Give the position of every P. falciparum parasite, noting its life-cycle stage.
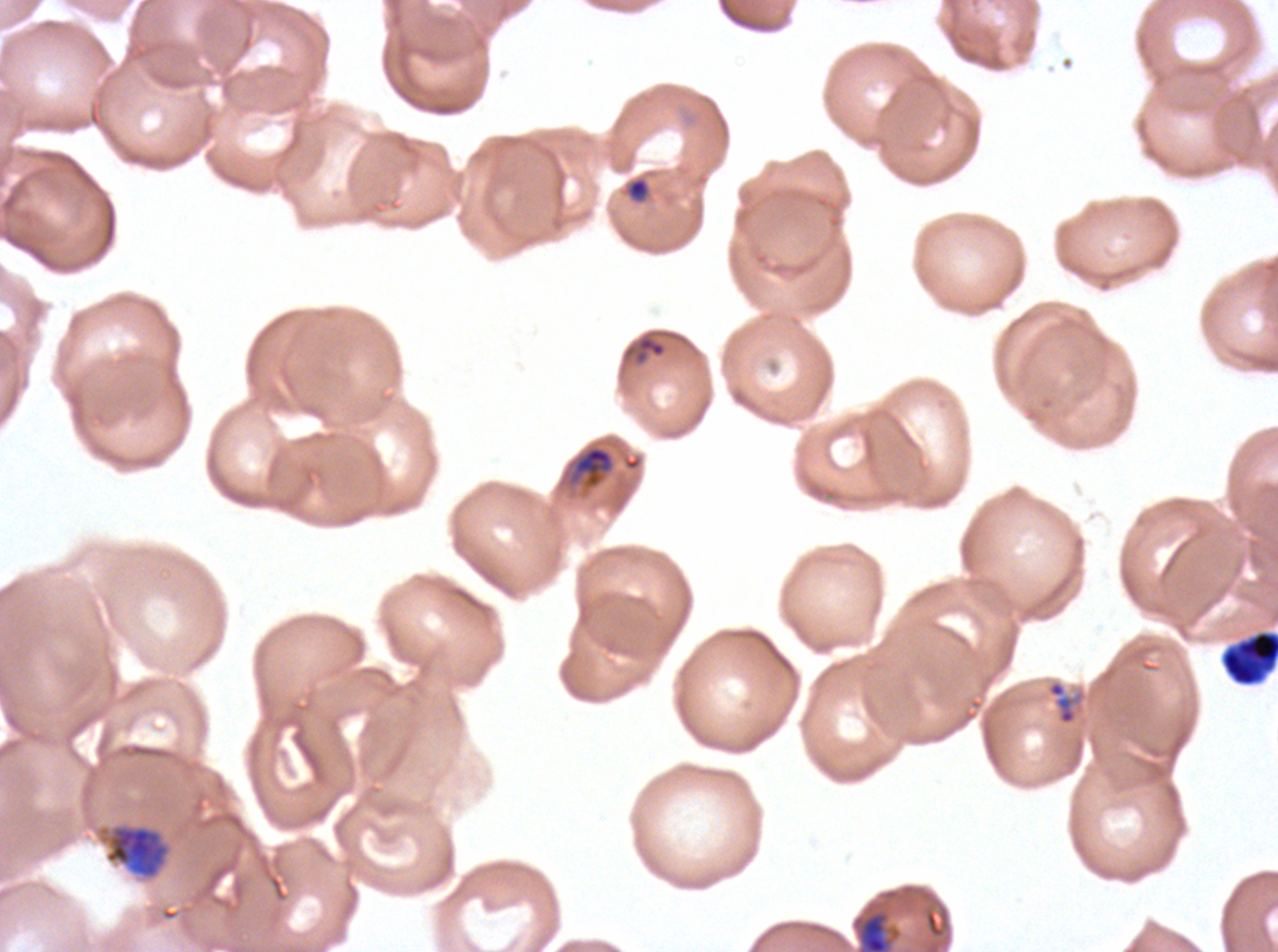

Approximate bounding boxes as (x1, y1, x2, y2) in pixels.
Rings: (635, 336, 667, 362).
Mid trophozoites: (573, 445, 614, 488), (852, 909, 902, 951).
Late trophozoites: (97, 824, 171, 880).
No late-ring/early-trophozoite forms, early schizonts, late schizonts, segmenters, or gametocytes observed.

debris locations = (622, 175, 652, 205), (1221, 629, 1277, 687), (1046, 679, 1087, 726)
preparation = thin blood film
stain = Giemsa
life-cycle stages observed = ring, mid trophozoite, late trophozoite
field of view = sub-image separated from a larger composite
image size = 1278×952 pixels
specimen = P. falciparum cultured ex vivo for 24 to 48 hours, from a patient in The Gambia